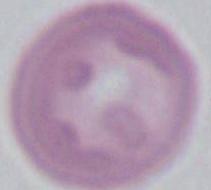
1000x magnification. Micrograph. An erythrocyte is seen.